Outline each Plasmodium parasite.
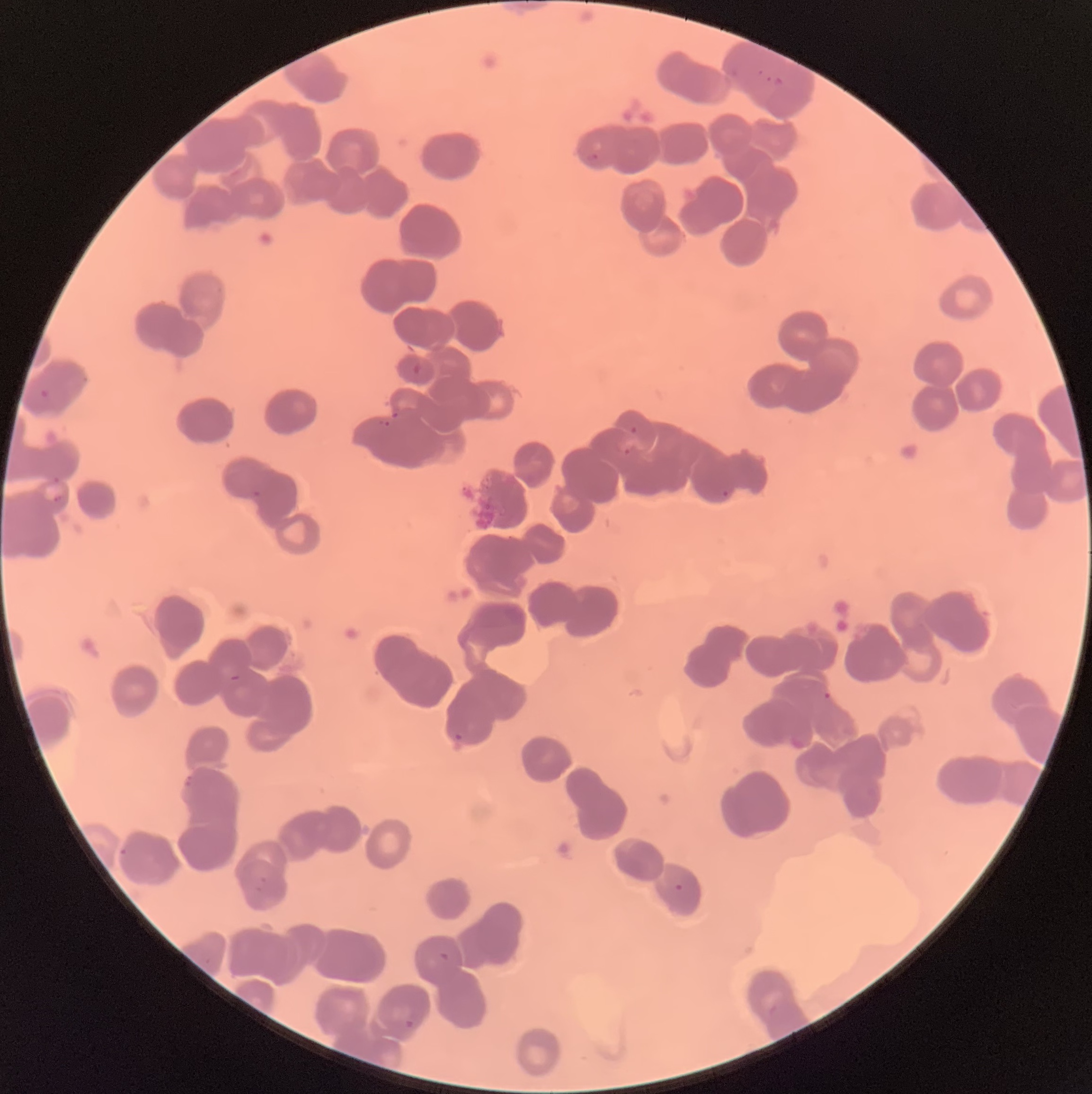

Approximate bounding boxes as (x1,y1)-(x2,y2) corner pairs in pixels.
Plasmodium parasites: (757,69)-(772,83), (586,153)-(598,160), (40,389)-(49,399), (378,420)-(390,427), (630,426)-(637,435), (614,441)-(636,456), (722,490)-(729,498), (52,495)-(64,505), (822,690)-(832,700), (452,733)-(463,739), (255,875)-(266,891), (673,883)-(684,891), (437,951)-(451,963), (402,1019)-(415,1028).

Image is 1092×1094 pixels. Optical microscopy. Thin blood smear. The red blood cells show rouleaux formation.